Assess the morphology of the red blood cells.
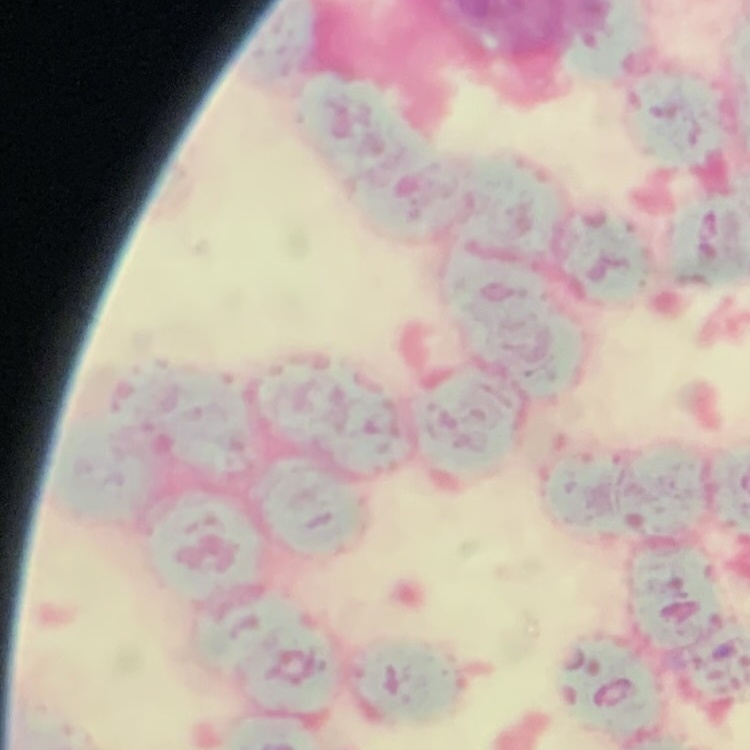
They show rouleaux formation.

preparation = thin blood smear
image type = square crop of a larger photomicrograph
stain = Field's or Giemsa